Assess this cell for malaria.
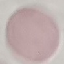

Uninfected.

Acquired by smartphone through the microscope eyepiece. Thin smear of blood. Cell patch, automatically extracted from a larger field of view and resized to 64 × 64 pixels. Giemsa-stained preparation.